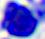 Captured at 400x magnification. Micrograph. A white blood cell is seen.